State which parasite is depicted.
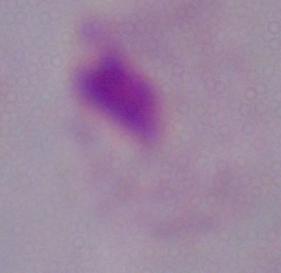
This is a trichomonad.

modality = micrograph
magnification = 1000x